Name the blood parasite species.
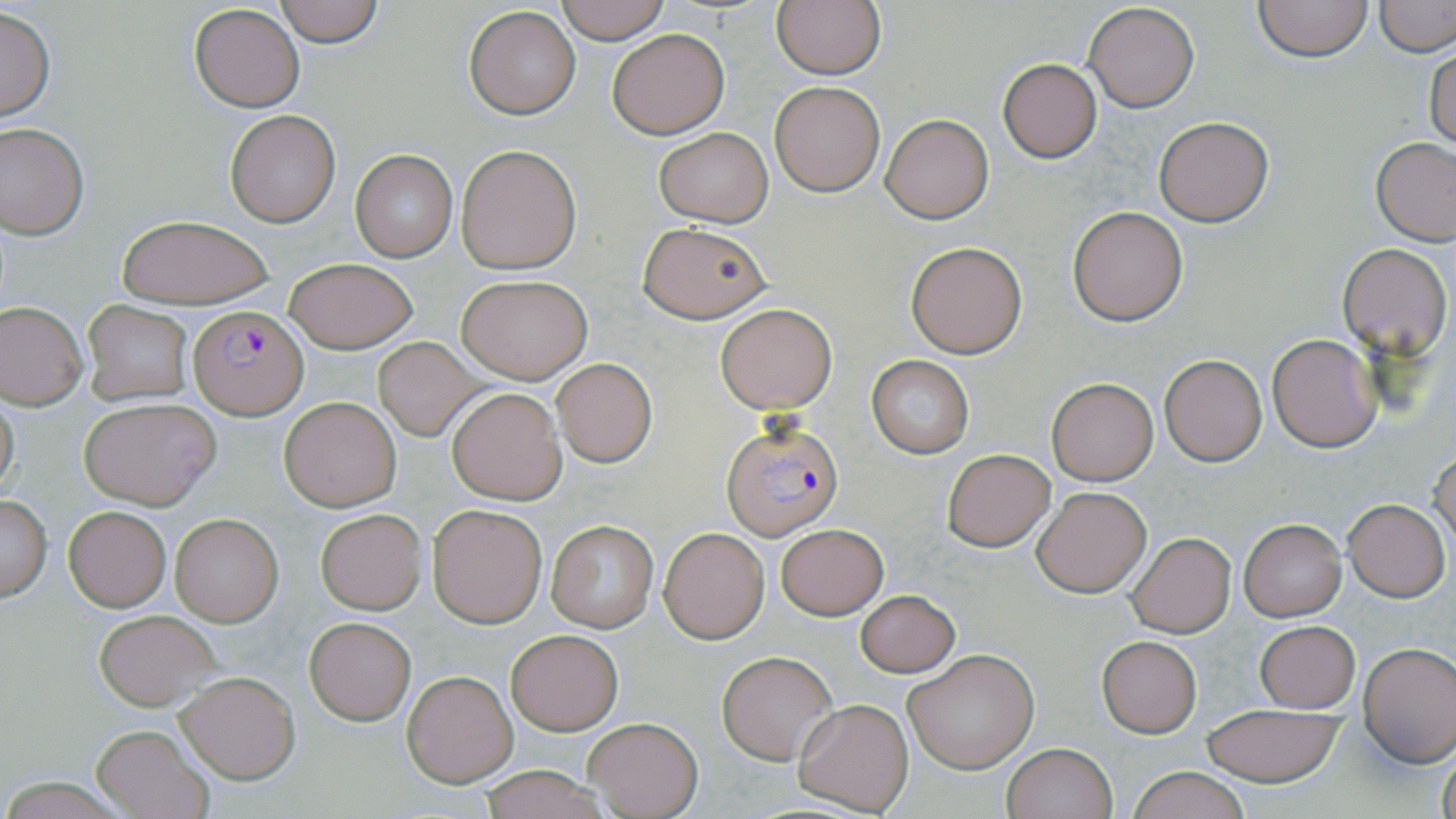
Plasmodium falciparum.

Approximate bounding boxes as [x1, y1, x2, y2] in pixels. Plasmodium falciparum-infected red blood cell locations: [188, 306, 308, 418], [722, 418, 843, 540]. Uninfected red blood cell locations: [274, 0, 384, 47], [554, 0, 670, 44], [771, 0, 886, 80], [1252, 0, 1375, 62], [1081, 1, 1199, 113], [1376, 1, 1454, 57], [189, 4, 304, 112], [0, 5, 56, 124], [463, 7, 581, 118], [607, 28, 728, 138], [1424, 43, 1456, 153], [996, 58, 1103, 163], [770, 80, 886, 197], [225, 111, 340, 227], [881, 113, 993, 223], [1152, 116, 1274, 226], [0, 122, 89, 239], [654, 128, 773, 227], [1372, 138, 1456, 246], [455, 145, 581, 274], [350, 149, 457, 262], [1069, 206, 1188, 325], [116, 216, 274, 308], [637, 222, 772, 323], [905, 241, 1027, 358], [1337, 243, 1452, 358], [284, 257, 418, 353], [457, 275, 592, 384], [82, 301, 192, 407], [1, 302, 87, 409], [716, 304, 836, 412], [1267, 333, 1382, 453], [371, 337, 483, 441], [1158, 354, 1267, 467], [866, 356, 974, 458], [551, 358, 657, 467], [1047, 378, 1158, 485], [448, 387, 566, 502], [0, 392, 20, 501], [278, 395, 401, 512], [78, 397, 222, 510], [1431, 447, 1456, 556], [942, 448, 1056, 552], [1032, 487, 1152, 598], [0, 494, 52, 601], [1342, 499, 1449, 601], [426, 502, 547, 628], [63, 505, 170, 612], [314, 507, 428, 615], [169, 511, 284, 627], [1239, 518, 1346, 620], [547, 520, 657, 632], [776, 524, 888, 619], [660, 528, 769, 642], [1125, 533, 1235, 638], [855, 589, 961, 678], [93, 610, 221, 710], [304, 618, 415, 723], [1254, 621, 1360, 712], [506, 629, 623, 735], [1096, 635, 1201, 738], [1359, 643, 1456, 765], [903, 647, 1041, 774], [716, 650, 837, 764], [403, 670, 517, 786], [175, 671, 299, 783], [795, 698, 914, 816], [1199, 702, 1347, 786], [583, 716, 704, 818], [91, 723, 213, 819], [1001, 742, 1117, 819], [1437, 745, 1456, 819], [1123, 766, 1256, 819], [477, 767, 610, 819]. Single field of view. Optical microscopy. May-Grünwald-Giemsa-stained preparation. Image is 1456×819 pixels. Captured at 1000x magnification. Thin blood film.